Describe the morphology of the erythrocytes.
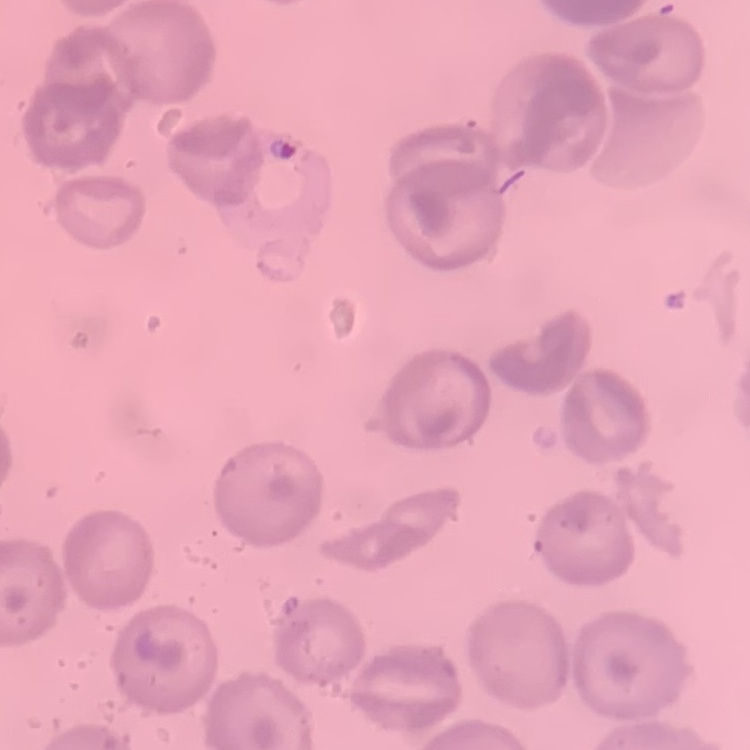

No rouleaux formation.

Summary:
  - Stain: Field's or Giemsa
  - Preparation: thin peripheral smear
  - Image type: square crop of a larger photomicrograph